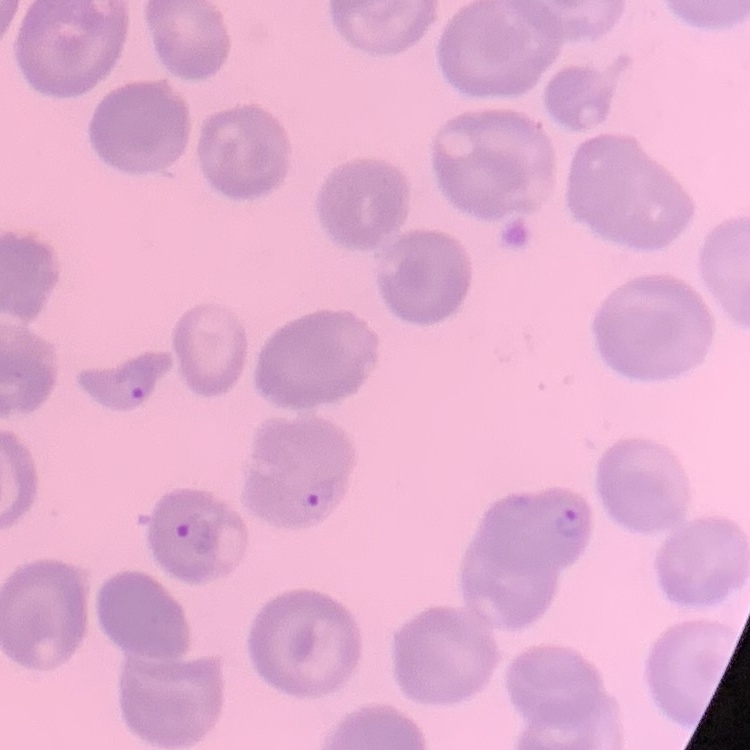

The erythrocytes show no rouleaux formation. Field's or Giemsa stain. Thin peripheral smear. One tile cut from a larger photomicrograph.